Identify the cell.
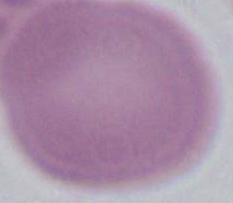
This is an erythrocyte.

Summary:
  - Magnification: 1000x
  - Modality: photomicrograph